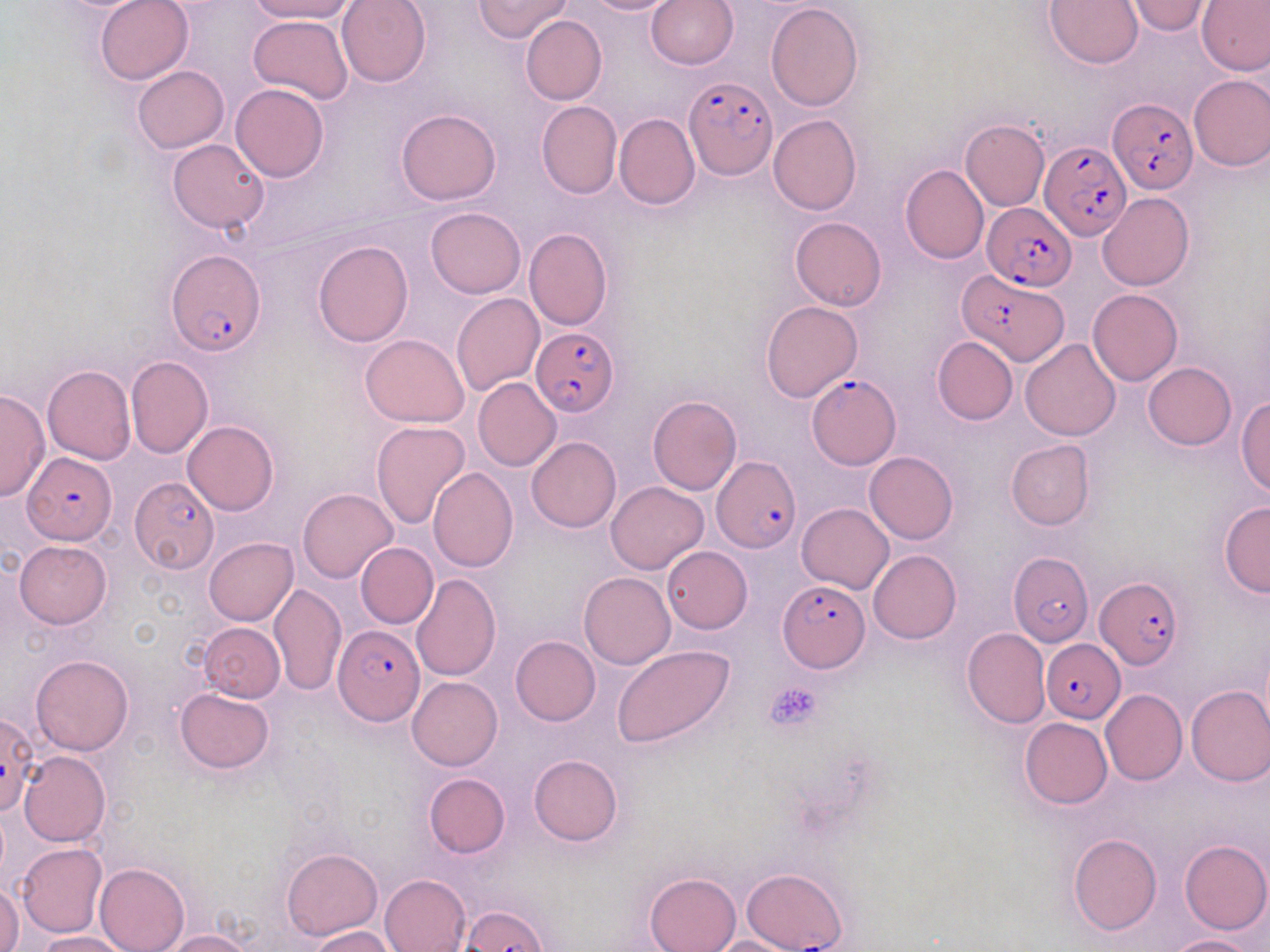

Approximate bounding boxes as (x1, y1, x2, y2) in pixels. Plasmodium falciparum-infected red blood cell locations: (685, 74, 779, 178), (1107, 98, 1196, 195), (1039, 140, 1134, 239), (982, 202, 1075, 289), (166, 251, 265, 356), (955, 269, 1064, 366), (532, 326, 619, 415), (808, 374, 900, 467), (21, 452, 116, 543), (712, 456, 800, 552), (130, 476, 219, 572), (1008, 551, 1094, 646), (1096, 577, 1182, 671), (776, 580, 869, 672), (334, 627, 424, 723), (1041, 638, 1125, 723), (0, 712, 37, 816), (741, 867, 849, 952). Uninfected red blood cell locations: (94, 0, 195, 85), (250, 0, 360, 22), (338, 0, 431, 87), (473, 0, 573, 43), (580, 0, 681, 15), (1046, 0, 1144, 69), (1123, 0, 1215, 35), (1197, 0, 1269, 74), (645, 1, 739, 71), (765, 2, 863, 111), (248, 15, 353, 104), (520, 15, 606, 105), (131, 65, 228, 152), (1188, 74, 1270, 170), (230, 83, 330, 183), (536, 101, 622, 199), (396, 108, 501, 204), (614, 113, 699, 211), (767, 114, 862, 214), (960, 119, 1049, 210), (167, 139, 269, 234), (900, 163, 989, 264), (1098, 193, 1194, 291), (425, 207, 526, 297), (790, 216, 886, 311), (523, 228, 612, 331), (312, 240, 413, 346), (1087, 289, 1183, 386), (452, 292, 545, 395), (761, 301, 862, 402), (361, 333, 470, 427), (931, 336, 1016, 426), (1020, 338, 1121, 441), (126, 356, 212, 458), (1143, 362, 1236, 450), (42, 365, 136, 465), (473, 378, 562, 471), (0, 388, 49, 502), (647, 396, 742, 496), (1236, 397, 1270, 499), (183, 421, 280, 515), (370, 421, 471, 530), (527, 437, 621, 532), (1005, 439, 1095, 531), (864, 451, 959, 543), (428, 467, 518, 571), (607, 482, 709, 574), (297, 488, 398, 583), (1218, 500, 1270, 597), (796, 503, 895, 593), (204, 537, 297, 626), (15, 540, 111, 627), (356, 543, 439, 628), (662, 547, 752, 633), (868, 550, 961, 644), (579, 571, 676, 669), (410, 573, 501, 681), (269, 583, 347, 695), (198, 622, 284, 702), (962, 628, 1050, 729), (511, 636, 600, 725), (611, 645, 735, 749), (31, 654, 134, 755), (407, 676, 503, 770), (1185, 683, 1270, 786), (175, 687, 274, 773), (1101, 689, 1188, 785), (1020, 717, 1112, 807), (20, 751, 111, 847), (528, 754, 622, 846), (423, 773, 509, 858), (1068, 834, 1162, 935), (1180, 839, 1270, 934), (15, 843, 107, 938), (282, 846, 382, 939), (95, 862, 190, 952), (645, 872, 741, 952), (379, 874, 471, 952), (0, 884, 22, 952), (309, 926, 397, 952), (165, 930, 253, 952), (36, 932, 131, 952), (700, 935, 806, 952), (1166, 935, 1258, 952). Platelet locations: (765, 680, 824, 730). Slide-level diagnosis: Plasmodium falciparum. Image is 1270×952 pixels. 1000x magnification. Thin blood film. Light microscopy. May-Grünwald-Giemsa-stained preparation. Single field of view.